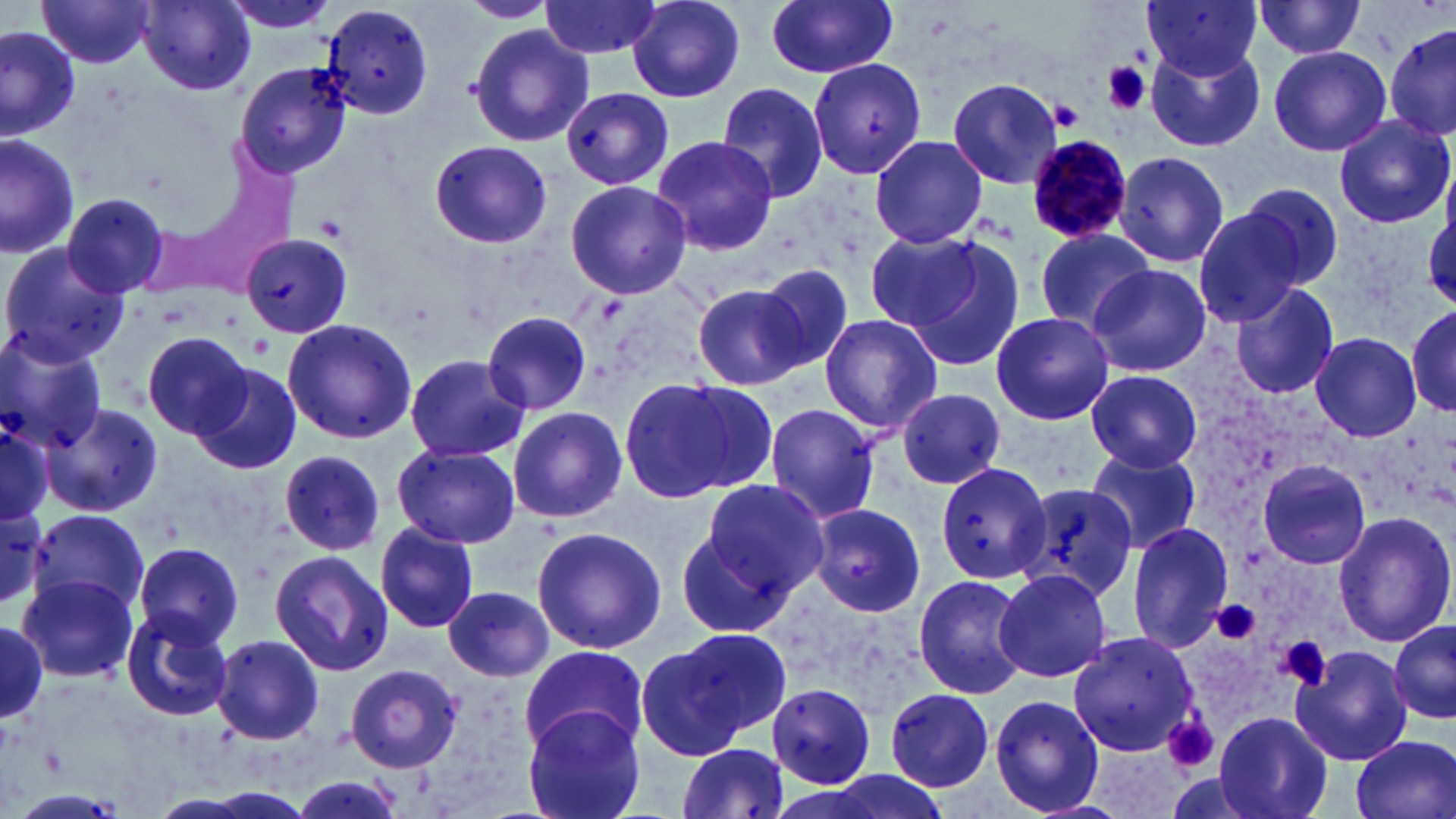
slide-level diagnosis = Plasmodium malariae
field of view = one of a larger specimen
modality = light microscopy
image size = 1456×819 pixels
platelet locations = approximate bounding boxes as (x1, y1, x2, y2) in pixels: (1103, 62, 1151, 115), (1053, 97, 1085, 129), (1216, 600, 1263, 644), (1283, 637, 1330, 691), (1165, 717, 1219, 773)
stain = May-Grünwald-Giemsa
Plasmodium malariae-infected red blood cell locations = approximate bounding boxes as (x1, y1, x2, y2) in pixels: (1025, 135, 1137, 244)
preparation = thin blood smear
magnification = 1000x
uninfected red blood cell locations = approximate bounding boxes as (x1, y1, x2, y2) in pixels: (140, 0, 255, 94), (219, 0, 339, 35), (459, 0, 555, 23), (765, 0, 899, 79), (1142, 0, 1263, 79), (37, 1, 158, 69), (538, 1, 663, 59), (626, 1, 747, 102), (1251, 2, 1370, 60), (321, 3, 437, 119), (1383, 22, 1456, 147), (469, 25, 592, 146), (0, 27, 78, 139), (1145, 44, 1266, 152), (1268, 46, 1391, 156), (806, 58, 929, 183), (234, 60, 352, 178), (947, 78, 1063, 189), (716, 81, 831, 205), (561, 87, 674, 191), (1333, 116, 1454, 229), (0, 133, 81, 260), (870, 134, 988, 247), (652, 136, 778, 252), (429, 140, 551, 248), (1113, 150, 1230, 269), (194, 174, 297, 291), (564, 179, 692, 300), (1236, 184, 1343, 291), (62, 191, 173, 300), (1191, 202, 1315, 327), (133, 216, 250, 299), (1033, 228, 1156, 332), (864, 229, 983, 330), (240, 234, 353, 335), (898, 236, 1025, 372), (0, 243, 128, 369), (754, 262, 856, 377), (1086, 264, 1210, 376), (693, 283, 810, 390), (1230, 283, 1341, 401), (1406, 303, 1455, 418), (481, 310, 592, 416), (989, 310, 1113, 424), (818, 313, 943, 433), (282, 318, 417, 446), (141, 330, 257, 439), (1310, 332, 1422, 441), (0, 333, 110, 452), (404, 353, 530, 463), (195, 362, 301, 476), (1086, 369, 1203, 472), (623, 377, 776, 501), (897, 388, 1005, 489), (44, 403, 163, 518), (764, 404, 882, 525), (507, 406, 627, 523), (0, 416, 53, 528), (393, 442, 519, 548), (1087, 447, 1203, 555), (280, 450, 385, 556), (1256, 459, 1372, 569), (935, 463, 1055, 585), (698, 478, 831, 599), (1013, 478, 1142, 604), (0, 499, 50, 607), (808, 503, 926, 616), (25, 507, 148, 622), (1330, 511, 1455, 647), (374, 520, 479, 633), (670, 521, 795, 635), (1126, 522, 1235, 649), (531, 525, 665, 654), (131, 541, 247, 649), (269, 550, 395, 677), (993, 569, 1111, 684), (915, 572, 1028, 696), (21, 574, 137, 681), (442, 585, 554, 683), (121, 609, 232, 721), (0, 617, 46, 726), (1388, 618, 1456, 726), (642, 630, 783, 756), (1067, 631, 1202, 757), (212, 634, 326, 746), (519, 645, 649, 754), (1291, 645, 1413, 766), (341, 661, 460, 772), (767, 684, 877, 788), (883, 688, 994, 790), (990, 695, 1105, 816), (519, 707, 648, 819), (1213, 710, 1334, 819), (1162, 713, 1222, 774), (1350, 734, 1455, 819), (675, 740, 792, 819), (284, 773, 407, 817)